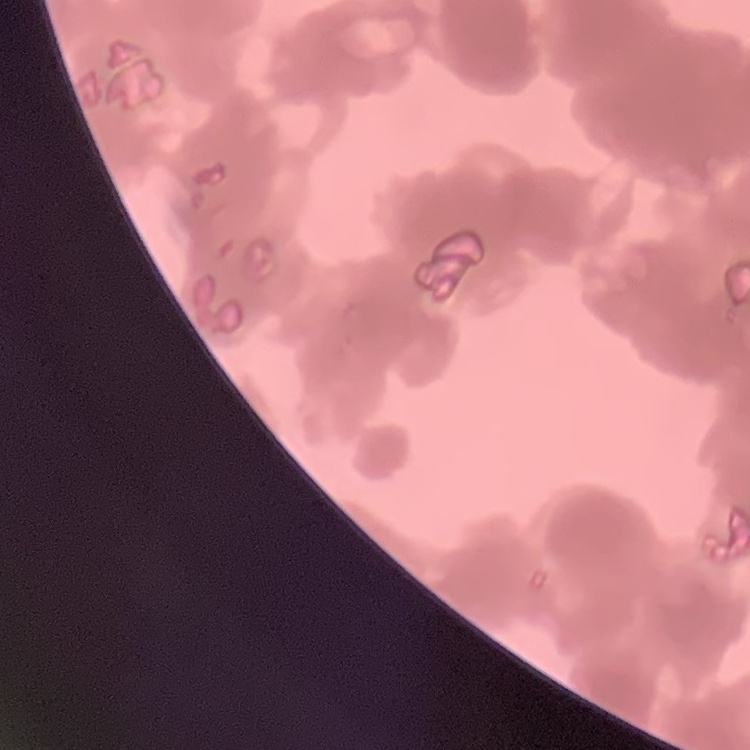
Summary:
  - Red blood cell morphology: rouleaux formation
  - Preparation: thin blood film
  - Image type: one tile cut from a larger photomicrograph
  - Stain: Field's or Giemsa